Locate every Plasmodium parasite.
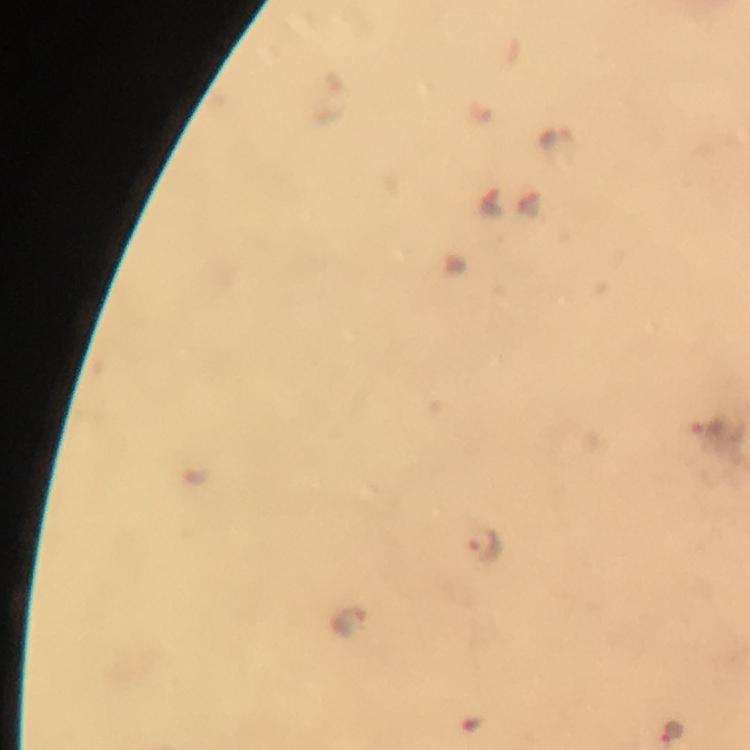
Approximate centers as {x, y} in pixels.
Plasmodium parasites: {485, 548}, {348, 621}, {670, 730}.

preparation: thick blood smear
cropped_from: a single field of view
capture: smartphone camera through the microscope
immersion_oil: used
magnification: 100x
context: from a diagnostic examination for malaria
image_size: 750×750 pixels
stain: Giemsa